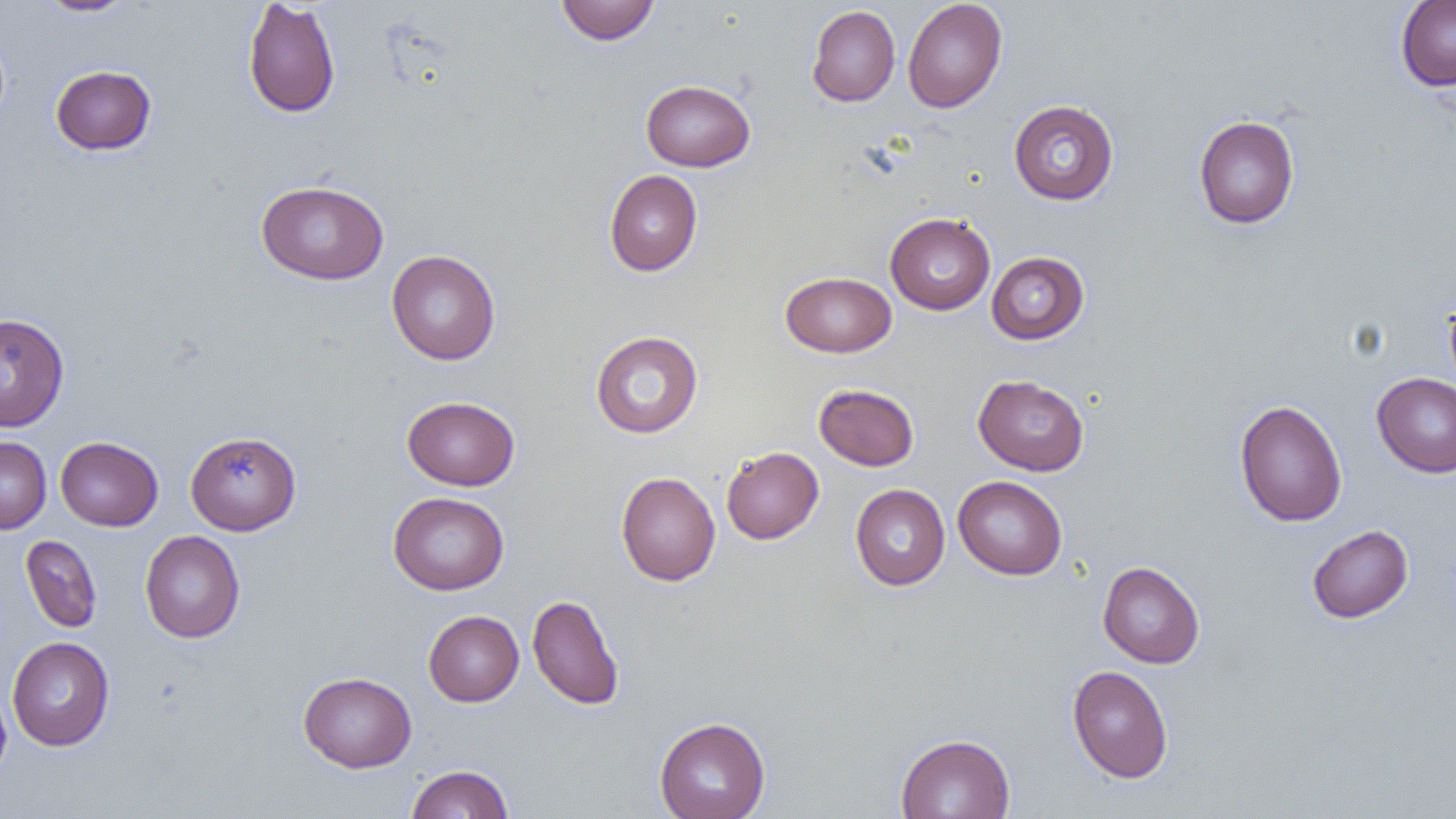
slide-level diagnosis = no evidence of blood parasites
magnification = 1000x
modality = light microscopy
preparation = thin blood film
image size = 1456×819 pixels
uninfected red blood cell locations = approximate bounding boxes as (x1,y1)-(x2,y2) corner pairs in pixels: (35,0)-(137,16), (243,0)-(341,118), (556,0)-(659,45), (902,0)-(1007,113), (1395,1)-(1456,91), (807,5)-(900,107), (50,65)-(156,155), (641,79)-(755,171), (1008,100)-(1119,205), (1193,115)-(1299,229), (604,170)-(702,276), (256,180)-(389,285), (885,212)-(996,315), (386,250)-(500,365), (986,251)-(1089,345), (780,271)-(896,357), (1443,291)-(1456,395), (0,312)-(69,431), (590,331)-(703,438), (1371,372)-(1456,478), (973,374)-(1089,476), (813,383)-(919,471), (402,396)-(520,491), (1234,399)-(1348,527), (185,431)-(301,534), (0,436)-(51,534), (55,436)-(163,531), (721,446)-(824,544), (616,471)-(720,586), (953,476)-(1067,580), (850,484)-(950,590), (388,491)-(509,595), (1307,524)-(1413,623), (140,530)-(245,643), (20,535)-(102,633), (1097,561)-(1205,669), (527,593)-(625,710), (423,610)-(524,706), (7,636)-(115,751), (1067,665)-(1174,783), (298,671)-(417,772), (0,680)-(12,785), (654,716)-(771,819), (895,733)-(1015,819), (405,764)-(514,819)
field of view = one of a larger specimen